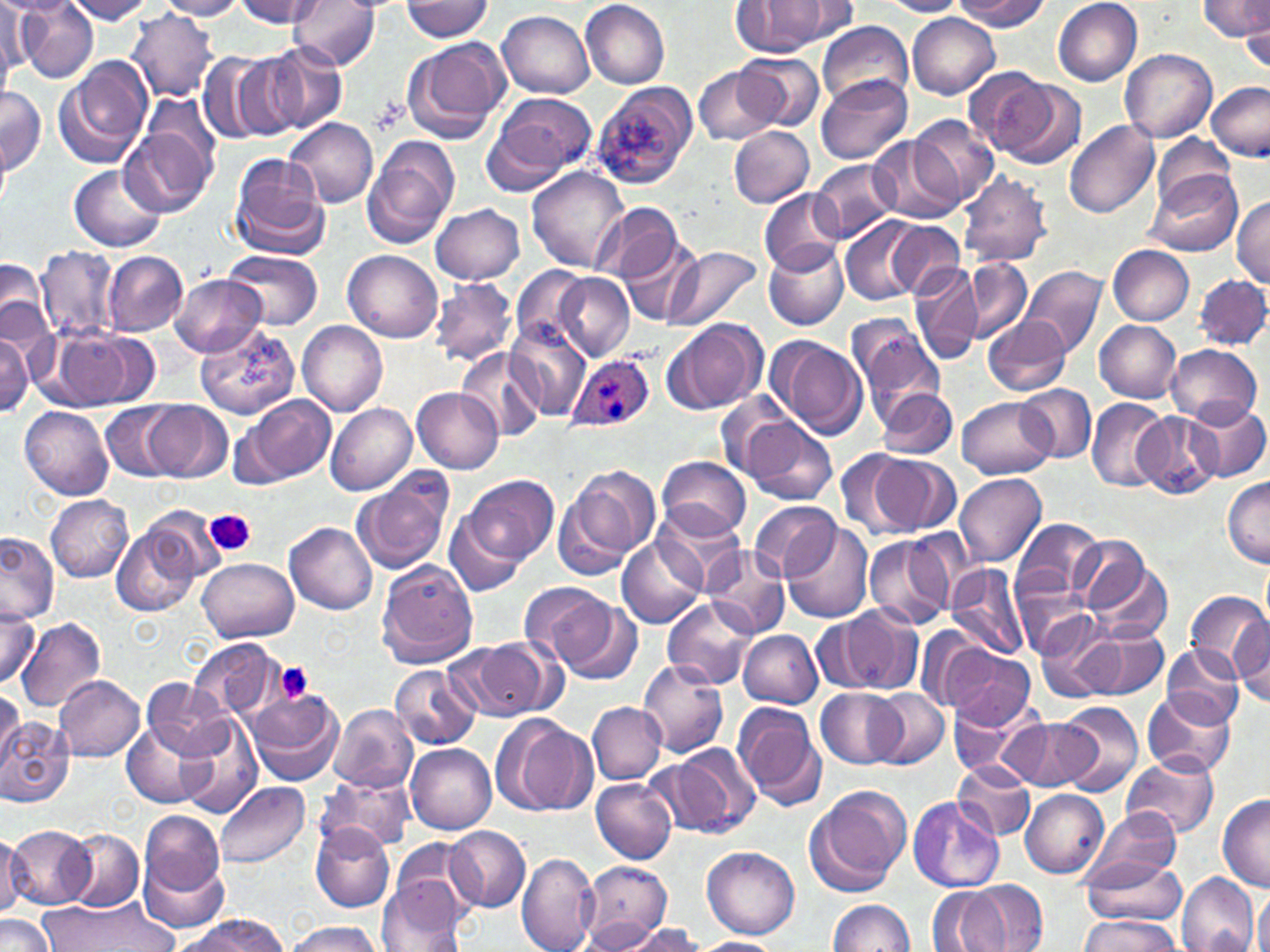 Approximate bounding boxes as (x1,y1)-(x2,y2) corner pairs in pixels. Platelet locations: (207,509)-(255,556), (274,661)-(313,703). Uninfected red blood cell locations: (0,0)-(78,19), (64,0)-(156,24), (157,0)-(248,20), (234,0)-(324,28), (288,0)-(382,71), (580,0)-(668,89), (883,0)-(966,17), (954,0)-(1048,31), (1052,0)-(1143,86), (1200,0)-(1269,42), (2,1)-(36,76), (403,1)-(496,41), (731,1)-(834,57), (780,1)-(857,42), (18,3)-(99,81), (126,9)-(220,102), (497,10)-(594,99), (1242,10)-(1270,71), (907,13)-(1000,99), (817,20)-(912,107), (403,36)-(510,143), (263,46)-(347,133), (1121,48)-(1217,143), (199,51)-(276,145), (227,54)-(306,142), (736,54)-(824,130), (55,58)-(152,169), (693,64)-(783,147), (963,69)-(1055,155), (815,76)-(913,165), (989,76)-(1086,168), (590,81)-(699,190), (1205,81)-(1270,161), (0,88)-(46,175), (484,90)-(596,189), (145,95)-(219,171), (909,114)-(1001,208), (284,118)-(379,209), (1065,118)-(1160,218), (120,124)-(213,217), (728,125)-(815,207), (868,136)-(963,224), (1149,136)-(1240,211), (363,138)-(460,247), (0,146)-(10,214), (230,157)-(329,259), (812,161)-(896,241), (69,165)-(167,253), (528,165)-(630,272), (1144,171)-(1243,257), (957,174)-(1053,267), (760,188)-(846,276), (1231,196)-(1270,287), (595,202)-(682,285), (431,203)-(525,285), (839,215)-(934,307), (884,221)-(965,298), (621,236)-(701,325), (764,242)-(848,330), (663,245)-(763,331), (1107,245)-(1194,325), (35,247)-(122,342), (223,249)-(324,328), (343,249)-(443,343), (103,251)-(189,335), (961,255)-(1033,342), (0,258)-(50,343), (510,265)-(591,350), (910,265)-(982,364), (1021,266)-(1106,359), (552,272)-(635,361), (1195,274)-(1270,350), (1186,275)-(1268,423), (172,276)-(265,357), (430,278)-(517,367), (846,314)-(945,422), (982,315)-(1071,396), (662,318)-(767,416), (297,320)-(387,417), (1095,320)-(1181,400), (505,322)-(591,421), (196,325)-(300,420), (57,331)-(144,406), (0,335)-(31,415), (767,335)-(868,439), (1166,344)-(1261,427), (457,347)-(546,441), (1015,384)-(1096,463), (412,387)-(504,473), (876,387)-(957,460), (716,394)-(815,493), (243,395)-(335,484), (958,398)-(1055,480), (1087,398)-(1170,494), (1185,400)-(1269,483), (147,401)-(231,483), (102,402)-(180,481), (325,402)-(416,496), (19,406)-(114,500), (1134,410)-(1221,499), (741,418)-(837,507), (835,448)-(920,542), (863,450)-(959,539), (658,455)-(752,539), (558,465)-(661,572), (955,472)-(1047,565), (465,473)-(558,563), (352,474)-(453,575), (1222,475)-(1270,565), (46,495)-(132,582), (747,501)-(840,580), (651,504)-(749,594), (445,508)-(526,597), (143,509)-(223,591), (1012,516)-(1103,607), (284,521)-(377,615), (782,521)-(874,624), (112,525)-(196,617), (1,532)-(58,623), (1070,532)-(1158,620), (863,533)-(957,629), (618,536)-(704,630), (703,546)-(791,638), (1087,557)-(1173,644), (198,558)-(299,642), (377,560)-(478,669), (947,564)-(1033,659), (1014,578)-(1096,661), (516,579)-(614,668), (1185,591)-(1269,677), (551,593)-(643,685), (663,597)-(759,691), (0,604)-(39,688), (823,605)-(924,695), (1231,614)-(1270,705), (1033,615)-(1129,702), (17,618)-(106,712), (1075,624)-(1170,701), (739,630)-(822,707), (187,638)-(282,722), (444,640)-(550,722), (938,643)-(1037,729), (1161,645)-(1243,726), (635,659)-(729,757), (389,665)-(479,749), (54,675)-(145,763), (140,680)-(230,761), (815,687)-(909,768), (0,688)-(22,775), (871,688)-(950,767), (1141,688)-(1237,779), (246,690)-(344,786), (948,697)-(1038,781), (733,701)-(824,809), (587,702)-(665,783), (1052,702)-(1144,796), (328,704)-(416,793), (176,715)-(261,817), (1001,717)-(1096,791), (0,718)-(75,807), (497,718)-(595,816), (121,719)-(213,809), (405,743)-(496,834), (672,743)-(761,836), (1123,756)-(1219,838), (952,760)-(1036,842), (316,773)-(414,852), (590,779)-(676,863), (214,782)-(310,869), (805,782)-(912,896), (1020,789)-(1110,878), (1216,795)-(1270,891), (908,797)-(1004,892), (1083,807)-(1181,888), (140,810)-(225,895), (311,822)-(395,912), (6,825)-(97,909), (445,826)-(530,911), (63,828)-(144,911), (0,831)-(23,918), (392,839)-(480,923), (702,846)-(799,938), (140,851)-(231,936), (517,852)-(599,952), (1079,855)-(1188,929), (579,860)-(673,948), (1176,872)-(1260,952), (377,878)-(469,952), (948,881)-(1048,951), (928,886)-(1003,951), (1254,888)-(1270,952), (39,897)-(176,951), (825,899)-(916,951), (0,915)-(56,952), (172,916)-(293,950), (1080,916)-(1185,951), (581,918)-(671,948), (287,920)-(382,952), (620,923)-(705,951), (692,937)-(788,952). Plasmodium ovale-infected red blood cell locations: (566,354)-(655,433). Slide-level diagnosis: Plasmodium ovale. Captured at 1000x magnification. Optical microscopy. May-Grünwald-Giemsa-stained preparation. Single field of view. Thin blood smear. Image is 1270×952 pixels.